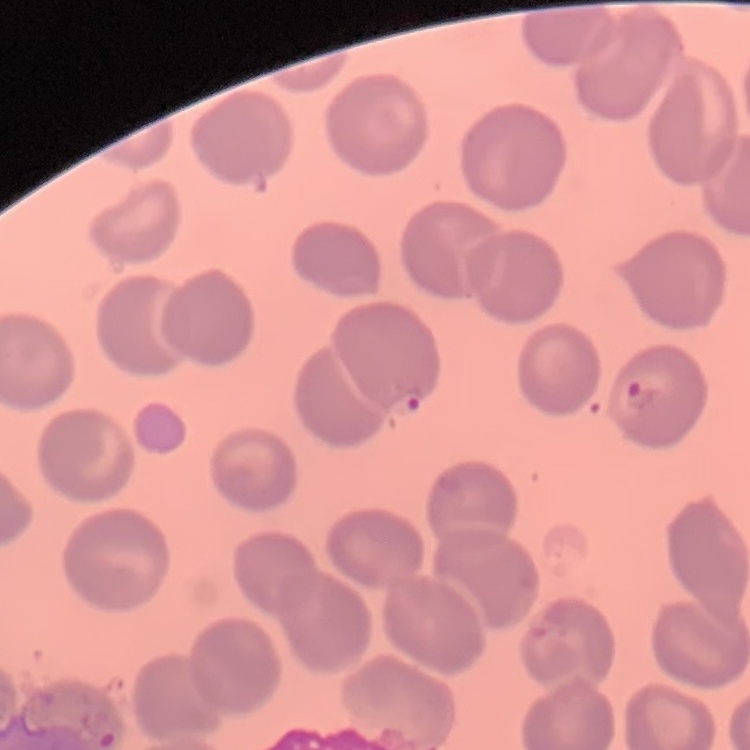
erythrocyte morphology = no rouleaux formation
stain = Field's or Giemsa
image type = one tile cut from a larger photomicrograph
preparation = thin blood film